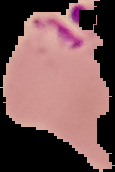
Segmented cell region on a black background. Malaria status: parasitized. Image is 115×172 pixels. From a thin blood film.